Name the parasite shown.
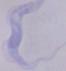

A trypanosome.

Summary:
  - Magnification: 1000x
  - Modality: micrograph